Name the blood parasite species.
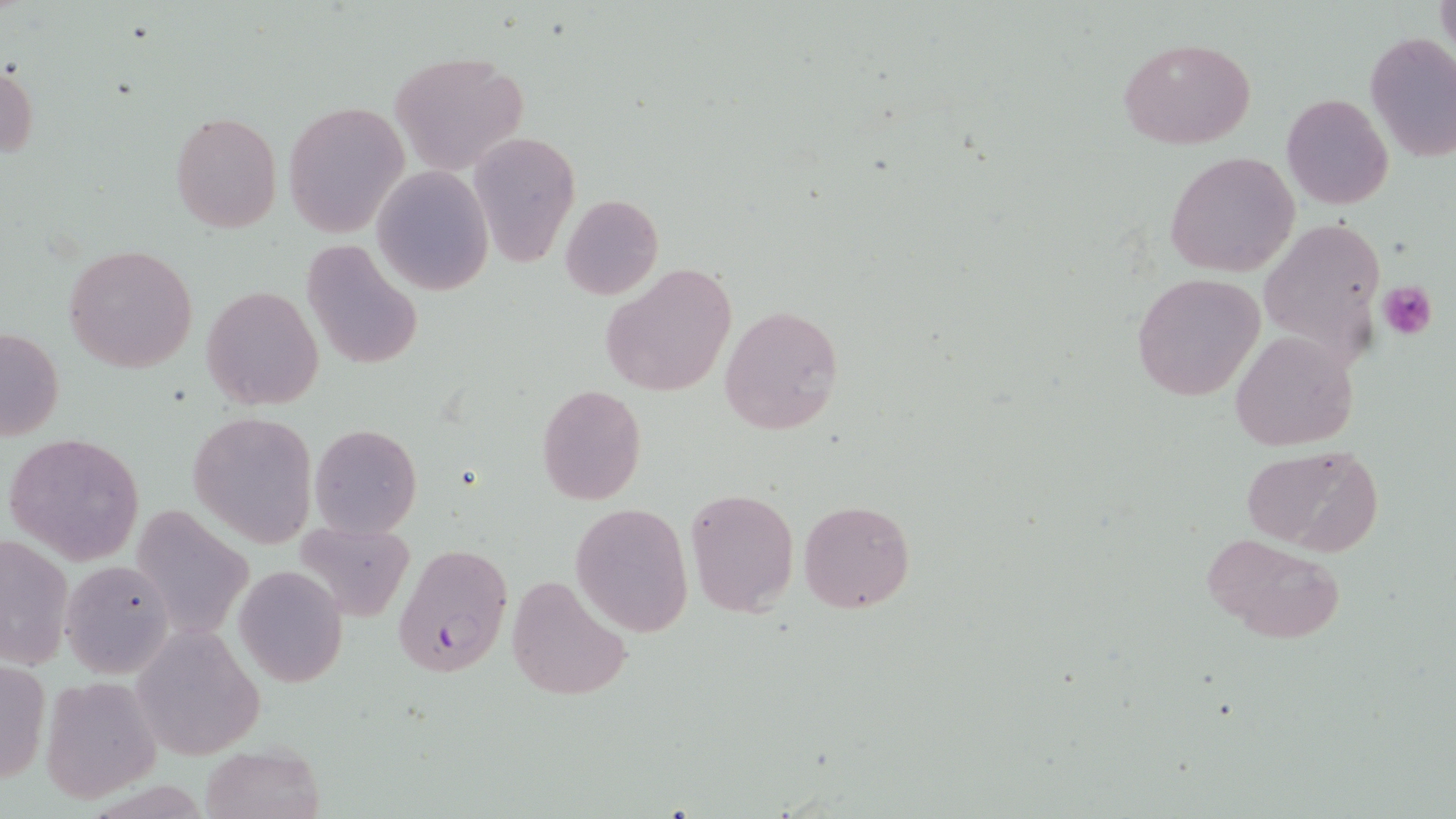
Plasmodium falciparum.

Summary:
  - Coordinate format: approximate bounding boxes as (x1,y1)-(x2,y2) corner pairs in pixels
  - Platelet locations: (1378,280)-(1437,340)
  - Uninfected red blood cell locations: (1435,0)-(1456,58), (1363,31)-(1456,166), (1119,36)-(1258,150), (388,53)-(529,176), (0,65)-(38,157), (1281,93)-(1394,210), (284,100)-(410,237), (169,111)-(282,231), (467,131)-(580,267), (1165,151)-(1300,278), (373,168)-(494,296), (560,193)-(663,300), (1258,216)-(1387,366), (302,240)-(424,373), (65,243)-(199,374), (601,261)-(736,397), (1131,272)-(1265,401), (201,285)-(323,409), (718,304)-(844,435), (0,324)-(64,444), (1230,331)-(1357,452), (536,384)-(647,505), (188,412)-(319,546), (310,424)-(422,537), (5,432)-(146,563), (1239,444)-(1382,552), (684,488)-(798,616), (798,499)-(916,613), (569,503)-(693,636), (292,520)-(415,622), (2,531)-(74,671), (1203,532)-(1348,645), (60,558)-(175,677), (234,563)-(349,688), (506,574)-(630,702), (132,627)-(265,756), (0,656)-(49,789), (40,676)-(161,804), (199,742)-(324,819)
  - Plasmodium falciparum-infected red blood cell locations: (395,545)-(513,675)
  - Magnification: 1000x
  - Modality: light microscopy
  - Field of view: single
  - Stain: May-Grünwald-Giemsa
  - Image size: 1456×819 pixels
  - Preparation: thin blood smear